Assess this cell for malaria.
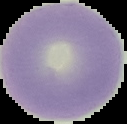
It is uninfected.

Image is 127×124 pixels. The area outside the segmented cell region is set to black. From a thin blood smear.